Classify this cell by malaria status.
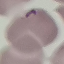

Uninfected.

Giemsa stain. Photographed with a smartphone camera at the microscope eyepiece. Cell patch, automatically extracted from a larger field of view and resized to 64 × 64 pixels. Thin smear of blood.